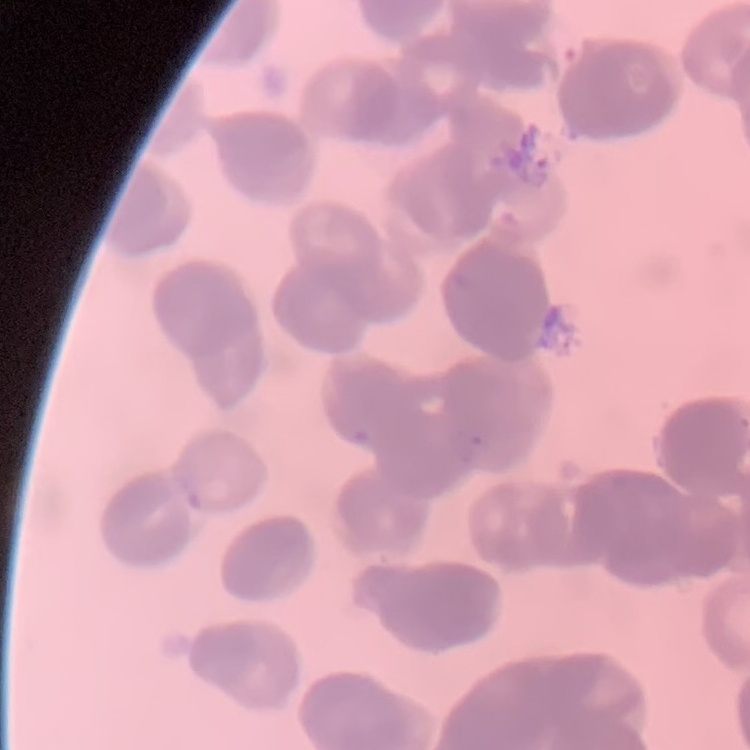

Summary:
  - Red blood cell morphology: rouleaux formation
  - Stain: Field's or Giemsa
  - Preparation: thin peripheral smear
  - Image type: square crop of a larger photomicrograph